Outline platelets.
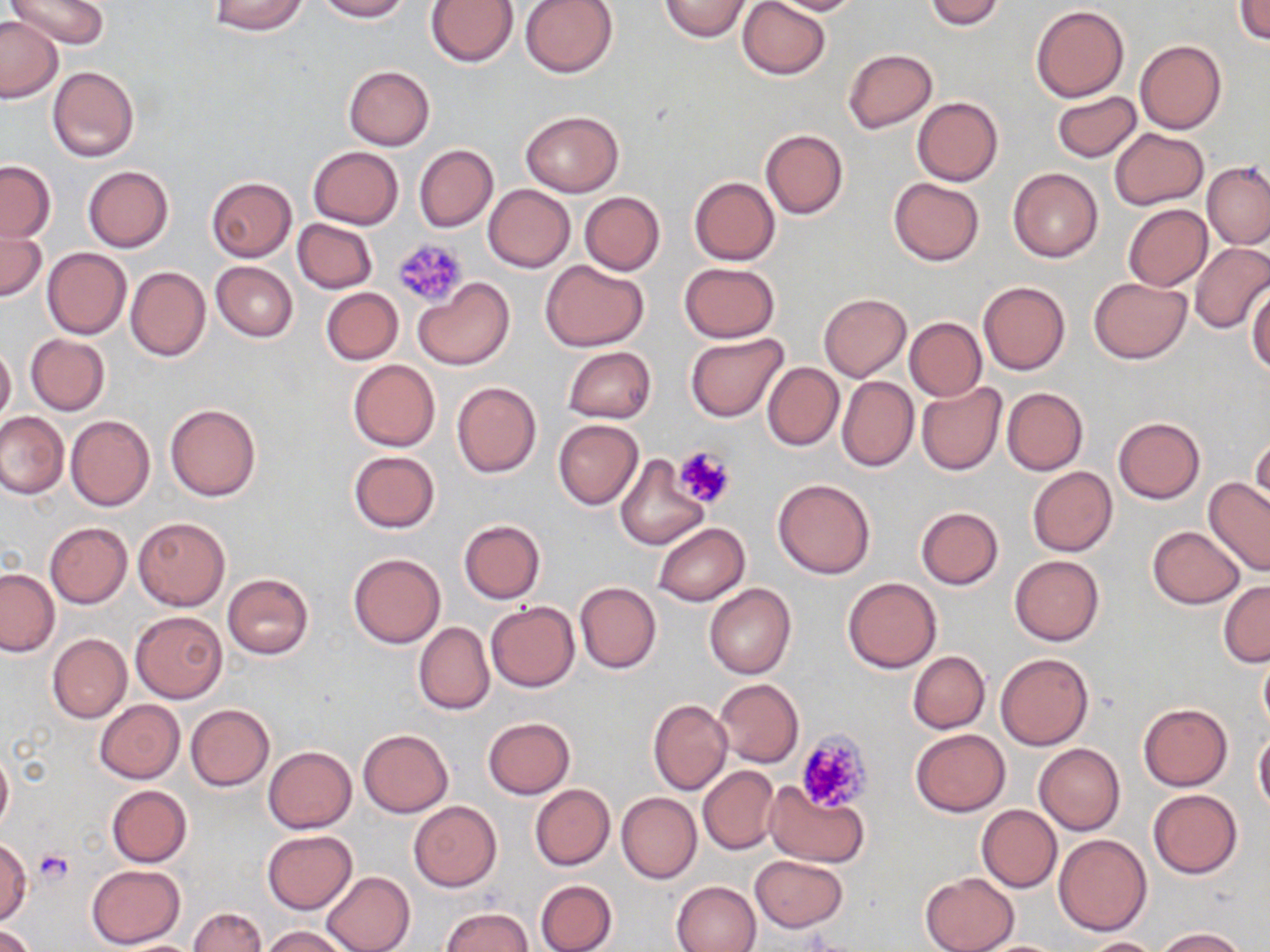
Approximate bounding boxes as (x1, y1, x2, y2) in pixels.
Platelets: (390, 236, 468, 309), (672, 446, 735, 508), (795, 730, 872, 812), (34, 850, 73, 886).

Uninfected red blood cell locations: (6, 0, 108, 51), (208, 0, 308, 35), (313, 0, 408, 21), (425, 0, 518, 68), (520, 0, 617, 78), (659, 0, 751, 42), (737, 0, 831, 79), (762, 0, 867, 15), (923, 0, 1006, 30), (1235, 0, 1270, 44), (1031, 5, 1129, 102), (0, 15, 63, 103), (1134, 40, 1227, 135), (843, 49, 938, 134), (343, 65, 435, 150), (47, 66, 138, 161), (1052, 91, 1142, 162), (913, 96, 1002, 185), (521, 111, 623, 196), (1109, 128, 1209, 210), (760, 129, 848, 219), (308, 145, 404, 229), (414, 145, 497, 231), (1, 161, 55, 242), (1204, 162, 1270, 250), (83, 165, 173, 252), (1007, 167, 1103, 262), (205, 176, 297, 262), (689, 176, 780, 264), (888, 178, 984, 265), (483, 185, 575, 271), (579, 192, 665, 275), (1124, 204, 1212, 291), (0, 218, 45, 304), (292, 218, 377, 293), (1189, 243, 1270, 335), (42, 247, 131, 338), (541, 261, 649, 351), (211, 262, 298, 341), (680, 262, 779, 342), (125, 266, 210, 361), (413, 277, 515, 370), (1088, 277, 1192, 364), (977, 280, 1070, 375), (1247, 283, 1270, 374), (320, 287, 403, 364), (818, 293, 910, 381), (903, 317, 987, 401), (25, 333, 110, 415), (686, 334, 789, 420), (0, 342, 15, 423), (563, 346, 656, 424), (348, 359, 440, 451), (762, 362, 843, 450), (838, 375, 919, 472), (451, 381, 542, 478), (915, 382, 1006, 475), (1002, 387, 1088, 474), (165, 403, 261, 502), (0, 411, 68, 499), (66, 415, 154, 510), (1113, 417, 1205, 503), (554, 419, 643, 509), (1249, 432, 1270, 516), (348, 450, 440, 533), (614, 455, 708, 551), (1028, 467, 1118, 557), (773, 478, 875, 578), (1204, 478, 1270, 576), (915, 506, 1004, 590), (133, 516, 229, 611), (458, 519, 545, 603), (44, 522, 132, 608), (653, 523, 750, 607), (1147, 526, 1244, 608), (348, 553, 446, 648), (1009, 555, 1104, 646), (1, 569, 59, 656), (222, 574, 314, 659), (843, 577, 940, 672), (575, 582, 661, 674), (1219, 582, 1270, 667), (704, 583, 796, 679), (485, 602, 581, 691), (130, 611, 228, 703), (413, 622, 494, 715), (47, 634, 131, 722), (1259, 645, 1270, 735), (907, 651, 990, 733), (995, 651, 1094, 750), (713, 678, 803, 768), (95, 699, 185, 784), (648, 699, 733, 795), (1138, 702, 1233, 791), (185, 704, 274, 790), (483, 717, 575, 799), (358, 728, 453, 817), (910, 728, 1010, 817), (1254, 732, 1270, 814), (1035, 744, 1125, 834), (0, 746, 12, 835), (263, 746, 357, 833), (697, 765, 780, 854), (764, 782, 868, 866), (530, 784, 614, 871), (106, 785, 193, 866), (1148, 789, 1243, 878), (616, 792, 702, 884), (409, 801, 501, 891), (977, 804, 1062, 892), (261, 829, 357, 913), (1054, 834, 1151, 935), (1, 839, 31, 925), (750, 855, 847, 932), (87, 865, 186, 948), (322, 871, 415, 952), (919, 872, 1018, 952), (535, 879, 617, 952), (672, 880, 762, 952), (188, 906, 266, 952), (440, 907, 533, 951), (0, 925, 37, 952), (263, 926, 351, 952), (1153, 927, 1249, 951), (1082, 937, 1162, 952). Slide-level diagnosis: negative for blood parasites. May-Grünwald-Giemsa-stained preparation. One field of a larger specimen. Thin blood smear. 1000x magnification. Optical microscopy. Image is 1270×952 pixels.